Locate every leukocyte (white blood cell).
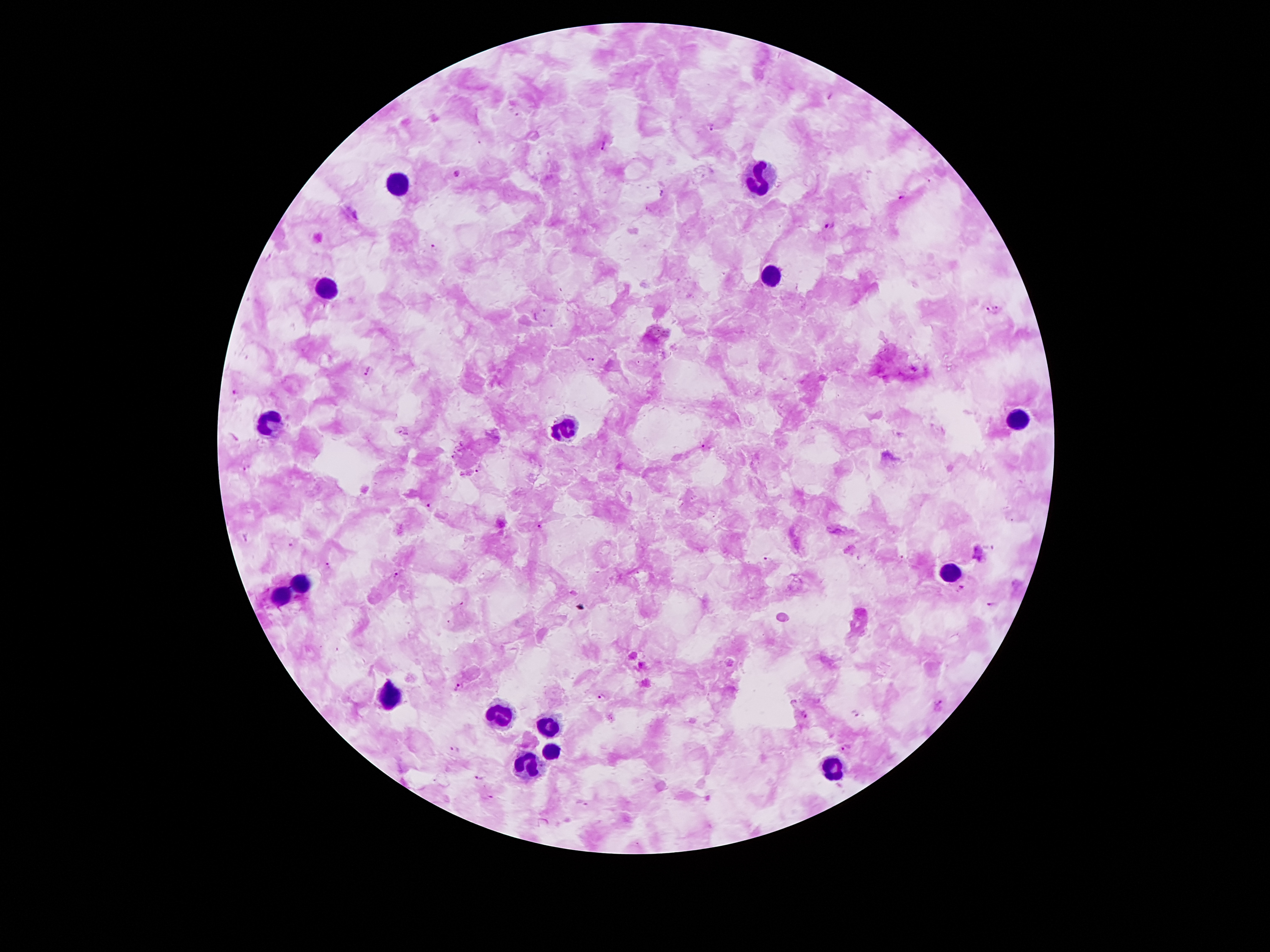

Approximate centers as [x, y] in pixels.
Leukocytes: [759, 175], [399, 182], [769, 277], [326, 289], [1015, 420], [269, 423], [567, 430], [947, 574], [301, 584], [283, 597], [392, 695], [501, 715], [549, 725], [552, 752], [527, 767], [835, 767].

Summary:
  - Malaria parasite locations: [712, 128], [604, 145], [457, 174], [900, 195], [830, 226], [435, 245], [997, 307], [989, 312], [591, 359], [368, 370], [235, 391], [704, 445], [248, 468], [477, 471], [428, 505], [539, 526], [245, 537], [291, 545], [766, 559], [328, 565], [396, 575], [962, 588], [993, 603], [457, 686], [603, 698], [939, 706], [857, 714], [805, 716], [845, 748], [455, 750], [481, 778], [490, 797], [584, 804]
  - Patient malaria status: infected with Plasmodium falciparum
  - Magnification: 100x
  - Preparation: thick blood smear
  - Field of view: one from this slide
  - Capture: smartphone through the microscope eyepiece
  - Image size: 1270×952 pixels
  - Stain: Giemsa